Classify this cell by malaria status.
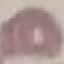

Uninfected.

image type = automatically extracted cell patch, resized to 64 × 64 pixels
preparation = thin blood film
stain = Giemsa
capture = smartphone camera at the microscope eyepiece